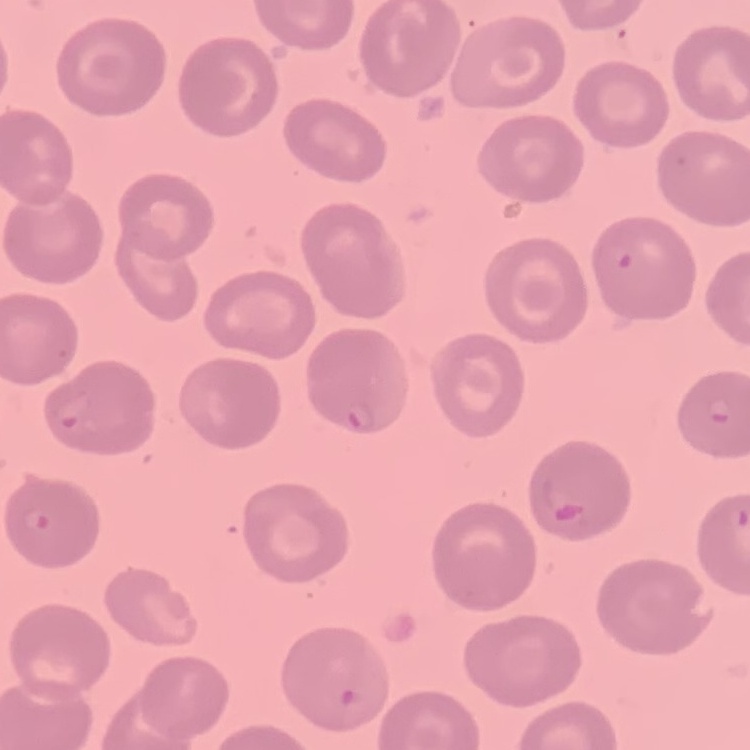
The erythrocytes show no rouleaux formation. One tile cut from a larger photomicrograph. Field's or Giemsa stain. Thin blood smear.